Assess this cell for malaria.
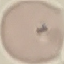

Uninfected.

{
  "capture": "smartphone through the microscope eyepiece",
  "preparation": "thin blood film",
  "image_type": "cell patch, automatically extracted from a larger field of view and resized to 64 × 64 pixels",
  "stain": "Giemsa"
}